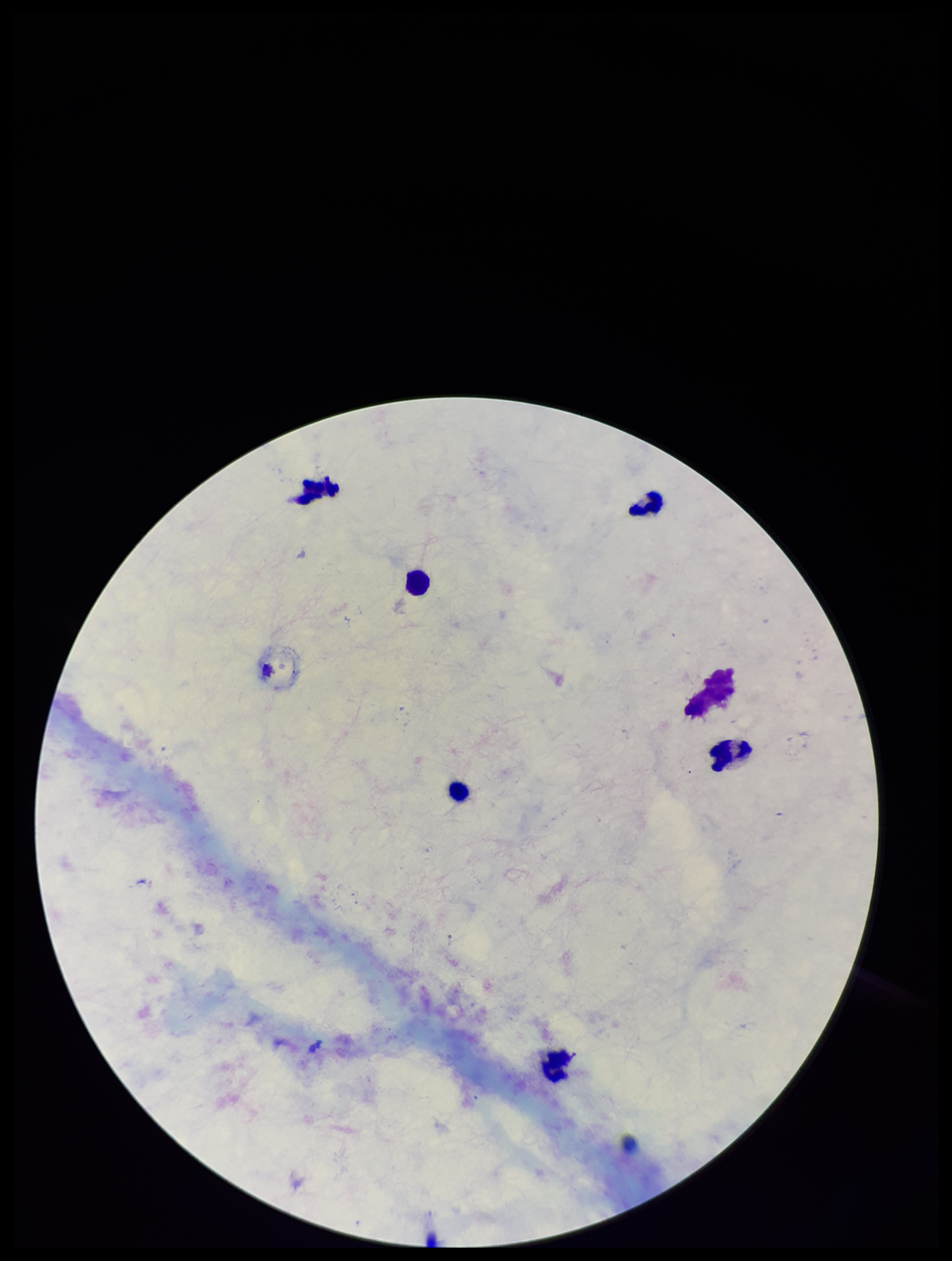
Single field of view. Patient malaria status: positive. Preparation: thick blood smear. Leukocyte count: 6. Species reported for this patient: Plasmodium falciparum. Plasmodium parasites: none detected. Giemsa stain. Smartphone photograph taken through the eyepiece of a microscope. Parasite count: 0. Image is 952×1261 pixels.